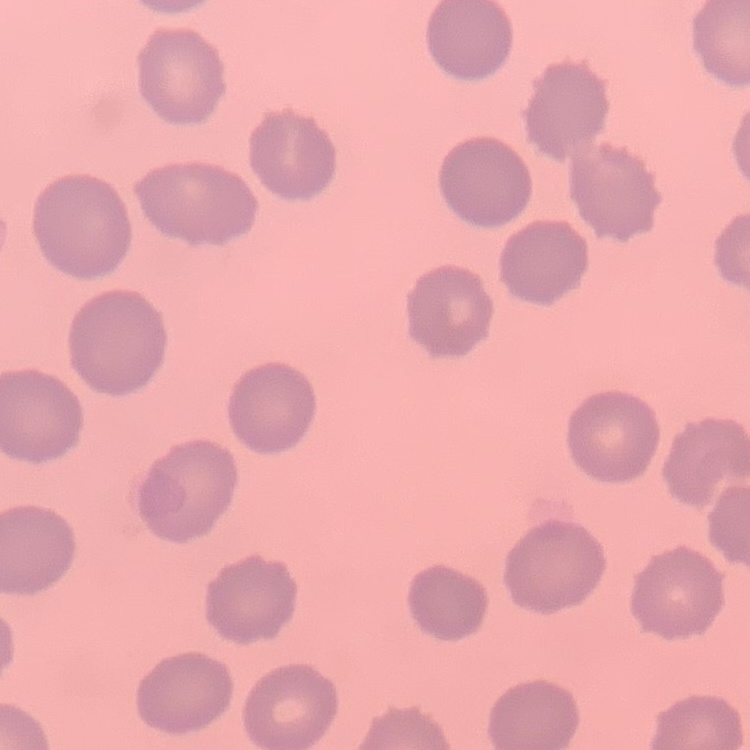

Summary:
  - Red blood cell morphology: no rouleaux formation
  - Preparation: thin peripheral smear
  - Stain: Field's or Giemsa
  - Image type: square crop of a larger photomicrograph